State which parasite is depicted.
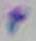

This is Toxoplasma gondii.

modality = micrograph
magnification = 1000x